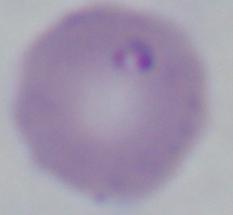
Summary:
  - Magnification: 1000x
  - Modality: photomicrograph
  - Identification: Babesia